Name the cell type shown.
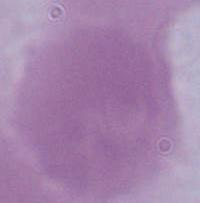

This is an erythrocyte.

Summary:
  - Magnification: 1000x
  - Modality: micrograph